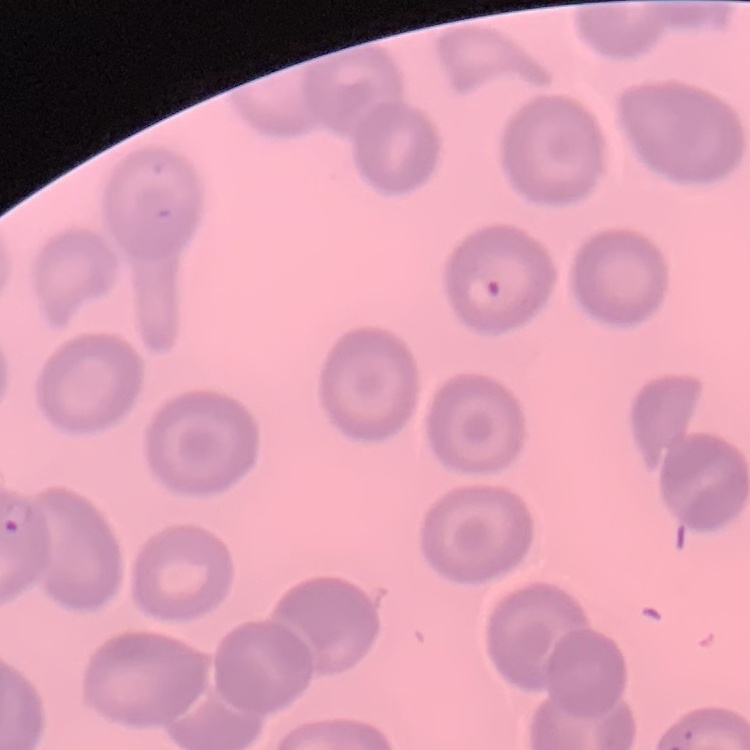
erythrocyte morphology = no rouleaux formation
stain = Field's or Giemsa
preparation = thin peripheral smear
image type = one tile cut from a larger photomicrograph